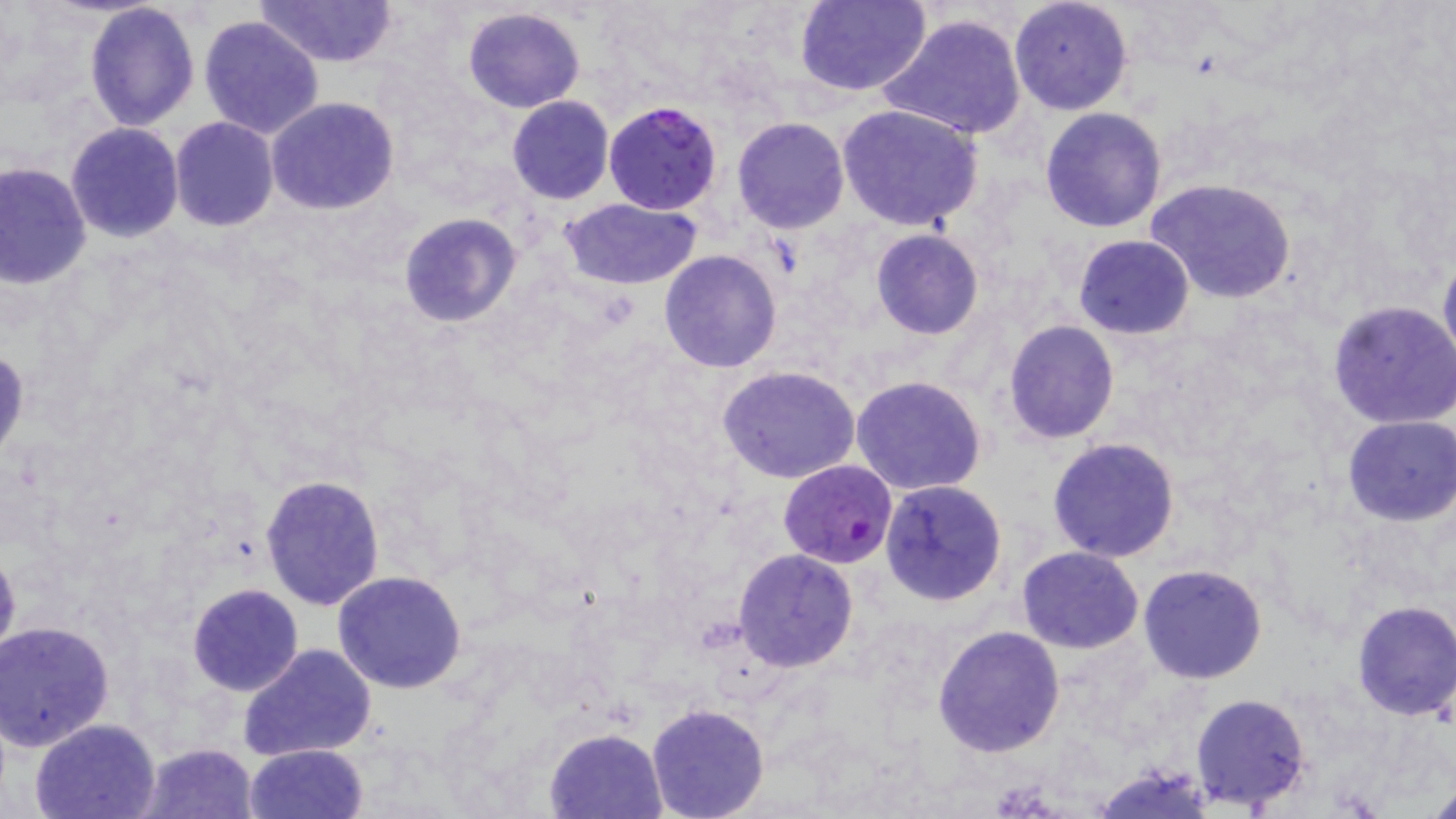

Summary:
  - Coordinate format: approximate bounding boxes as (x1, y1, x2, y2) in pixels
  - Uninfected red blood cell locations: (254, 0, 397, 67), (1009, 0, 1134, 116), (794, 1, 932, 97), (83, 3, 200, 132), (462, 6, 586, 113), (879, 12, 1029, 141), (198, 14, 325, 139), (506, 96, 614, 204), (266, 97, 400, 216), (838, 104, 986, 232), (1039, 106, 1167, 231), (169, 117, 278, 232), (732, 117, 850, 234), (64, 122, 183, 243), (0, 160, 92, 288), (1148, 178, 1296, 303), (559, 198, 705, 289), (398, 212, 521, 328), (871, 229, 984, 340), (1074, 234, 1195, 339), (659, 250, 782, 373), (1438, 250, 1456, 379), (1327, 300, 1456, 428), (1003, 318, 1119, 443), (0, 345, 28, 461), (718, 365, 860, 484), (851, 374, 988, 496), (1341, 415, 1454, 526), (1047, 437, 1181, 563), (260, 474, 385, 612), (879, 479, 1007, 607), (0, 543, 21, 673), (1017, 546, 1143, 653), (732, 549, 859, 671), (1138, 564, 1269, 684), (333, 571, 468, 695), (188, 584, 303, 695), (1350, 600, 1456, 721), (1, 622, 117, 755), (933, 626, 1065, 757), (238, 642, 378, 762), (1189, 692, 1313, 809), (646, 704, 770, 819), (30, 717, 161, 819), (545, 728, 666, 817), (135, 742, 260, 819), (243, 743, 368, 819), (1091, 761, 1217, 817)
  - Plasmodium falciparum-infected red blood cell locations: (604, 100, 724, 215), (776, 456, 898, 570)
  - Slide-level diagnosis: Plasmodium falciparum
  - Image size: 1456×819 pixels
  - Stain: May-Grünwald-Giemsa
  - Preparation: thin blood smear
  - Modality: light microscopy
  - Field of view: one of a larger specimen
  - Magnification: 1000x